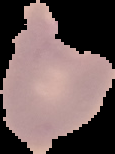
Summary:
  - Image size: 115×154 pixels
  - Preparation: thin blood film
  - Image type: cell region segmented out of the field of view; surrounding area masked to black
  - Result: malaria parasites detected